Describe the morphology of the red blood cells.
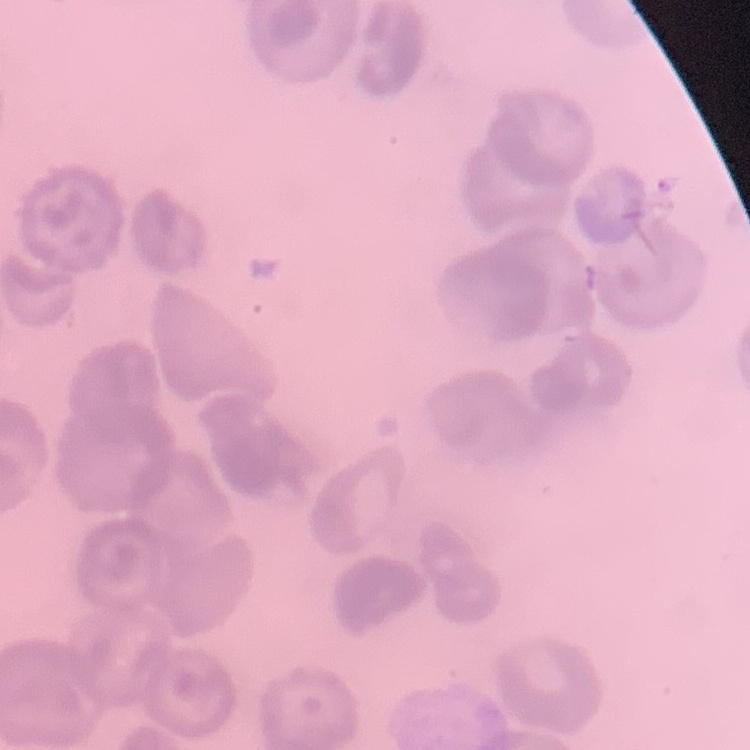
No rouleaux formation.

One tile cut from a larger photomicrograph. Thin blood smear. Field's or Giemsa stain.